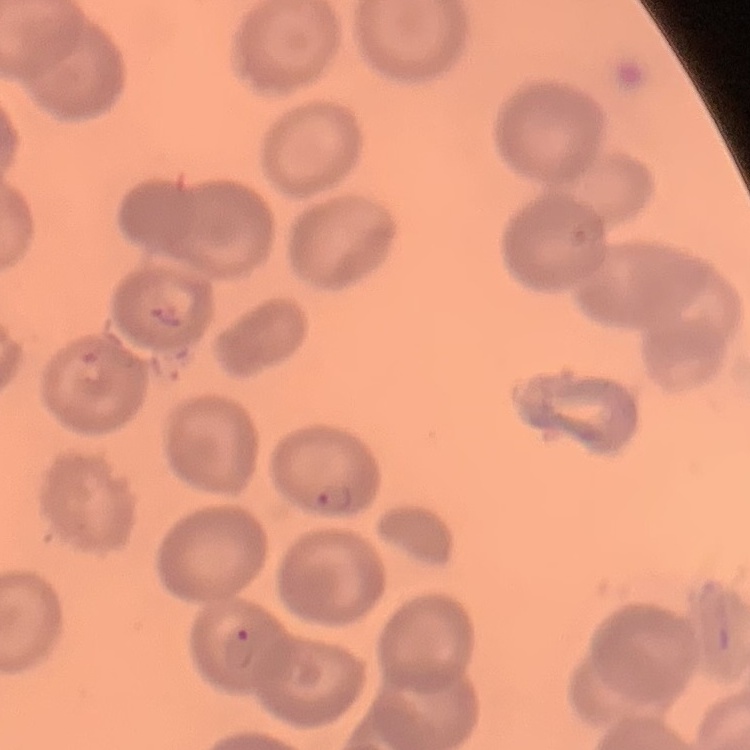

red blood cell morphology = no rouleaux formation
stain = Field's or Giemsa
image type = square crop of a larger photomicrograph
preparation = thin peripheral smear